State which parasite is depicted.
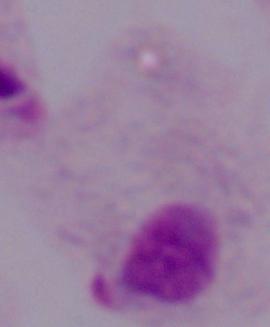
This is a trichomonad.

Summary:
  - Modality: micrograph
  - Magnification: 1000x